State the preparation type.
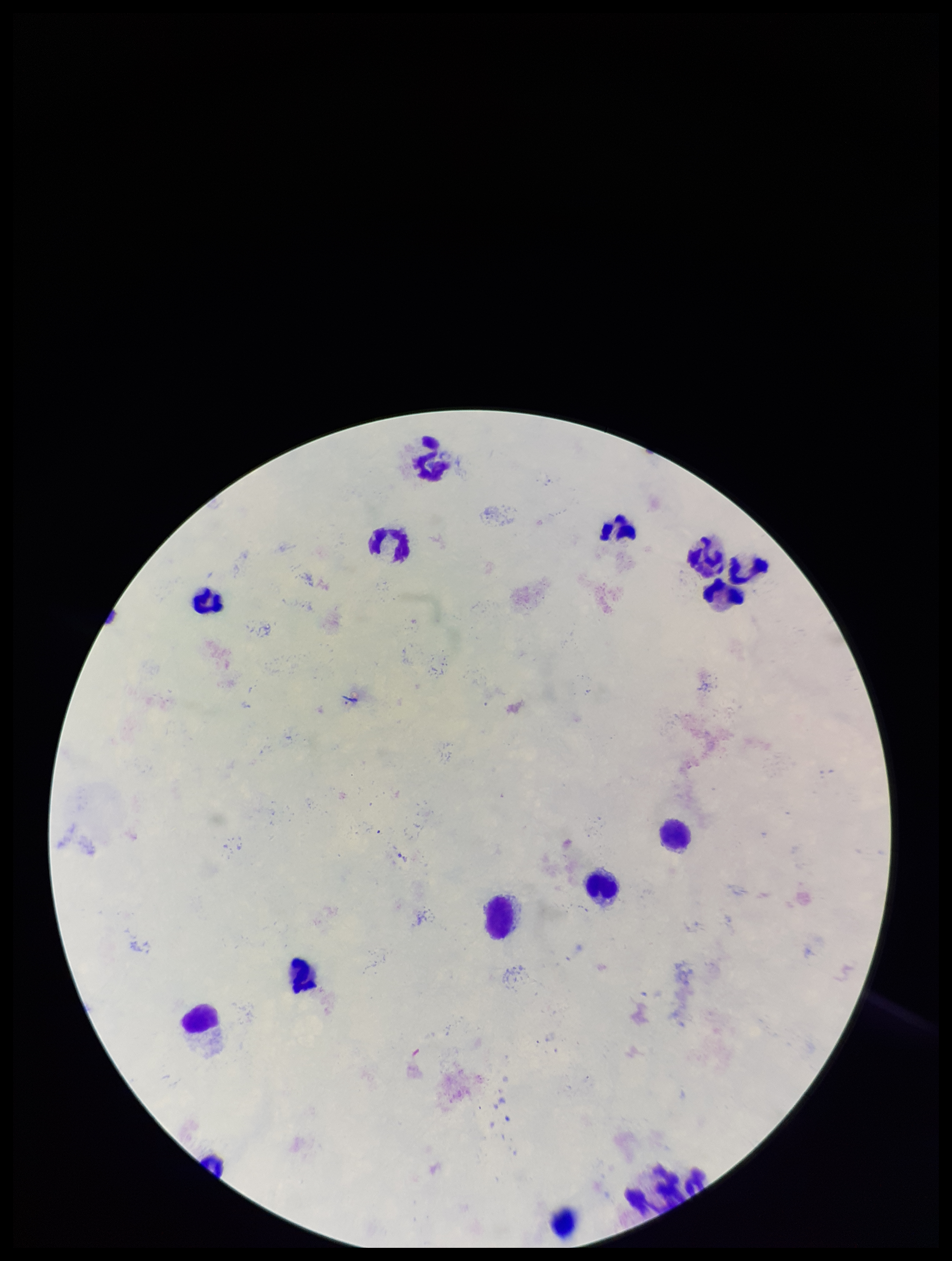

A thick smear.

Summary:
  - Plasmodium parasites: none seen
  - Patient malaria status: negative
  - Stain: Giemsa
  - Parasite count: 0
  - Field of view: one from this slide
  - Image size: 952×1261 pixels
  - Capture: smartphone photograph through the microscope eyepiece
  - Leukocyte count: 15